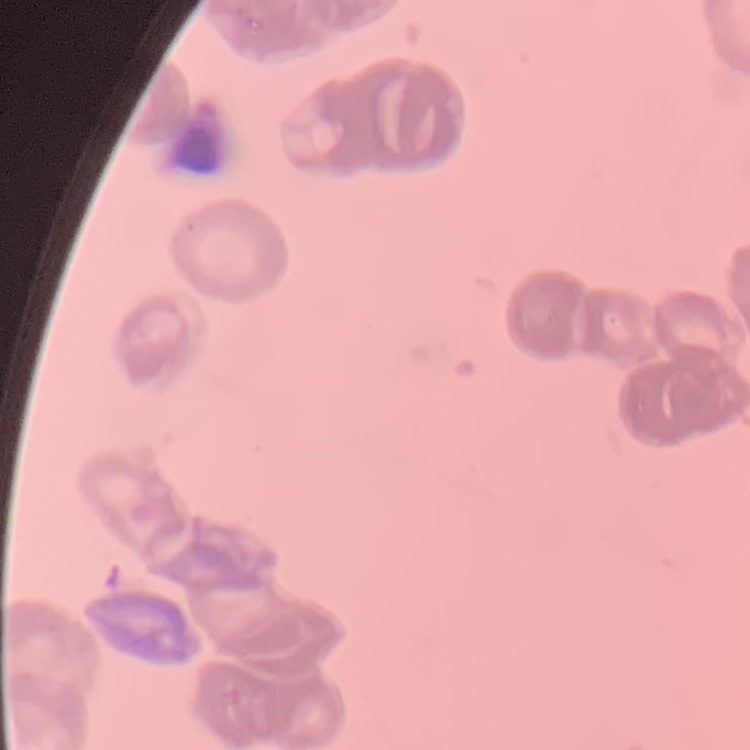

The red blood cells exhibit rouleaux formation. Stained with either Field's or Giemsa. Thin peripheral smear. Square crop of a larger photomicrograph.